State which parasite is depicted.
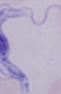

A trypanosome.

Micrograph. Captured at 1000x magnification.